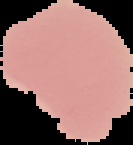
Summary:
  - Image type: segmented cell region on a black background
  - Preparation: thin blood smear
  - Malaria status: uninfected
  - Image size: 133×145 pixels